Point out each Plasmodium parasite.
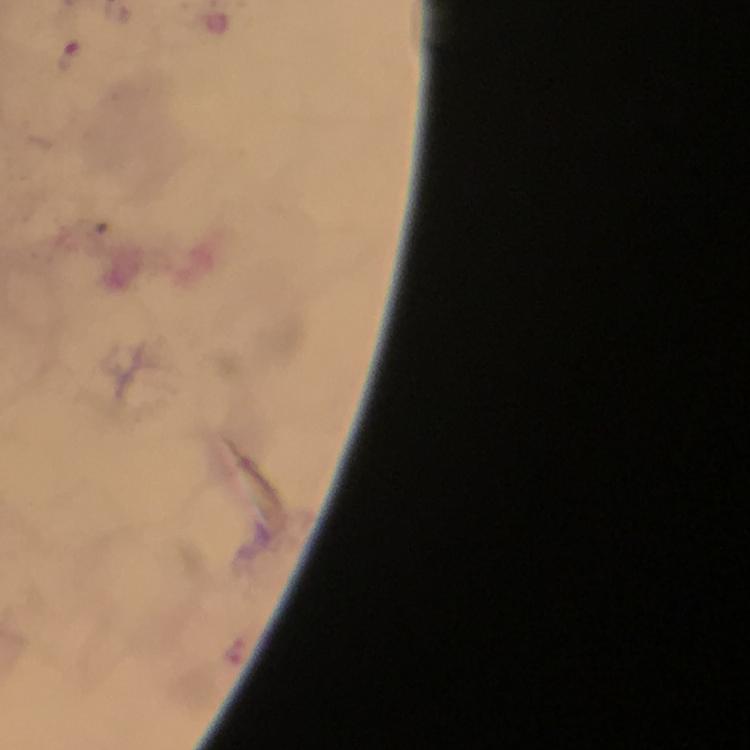

Approximate centers as {x, y} in pixels.
Plasmodium parasites: {69, 55}.

context = from a diagnostic examination for malaria
preparation = thick smear
image size = 750×750 pixels
magnification = 100x
cropped from = a single field of view
stain = Giemsa
capture = smartphone photograph through a microscope
immersion oil = used